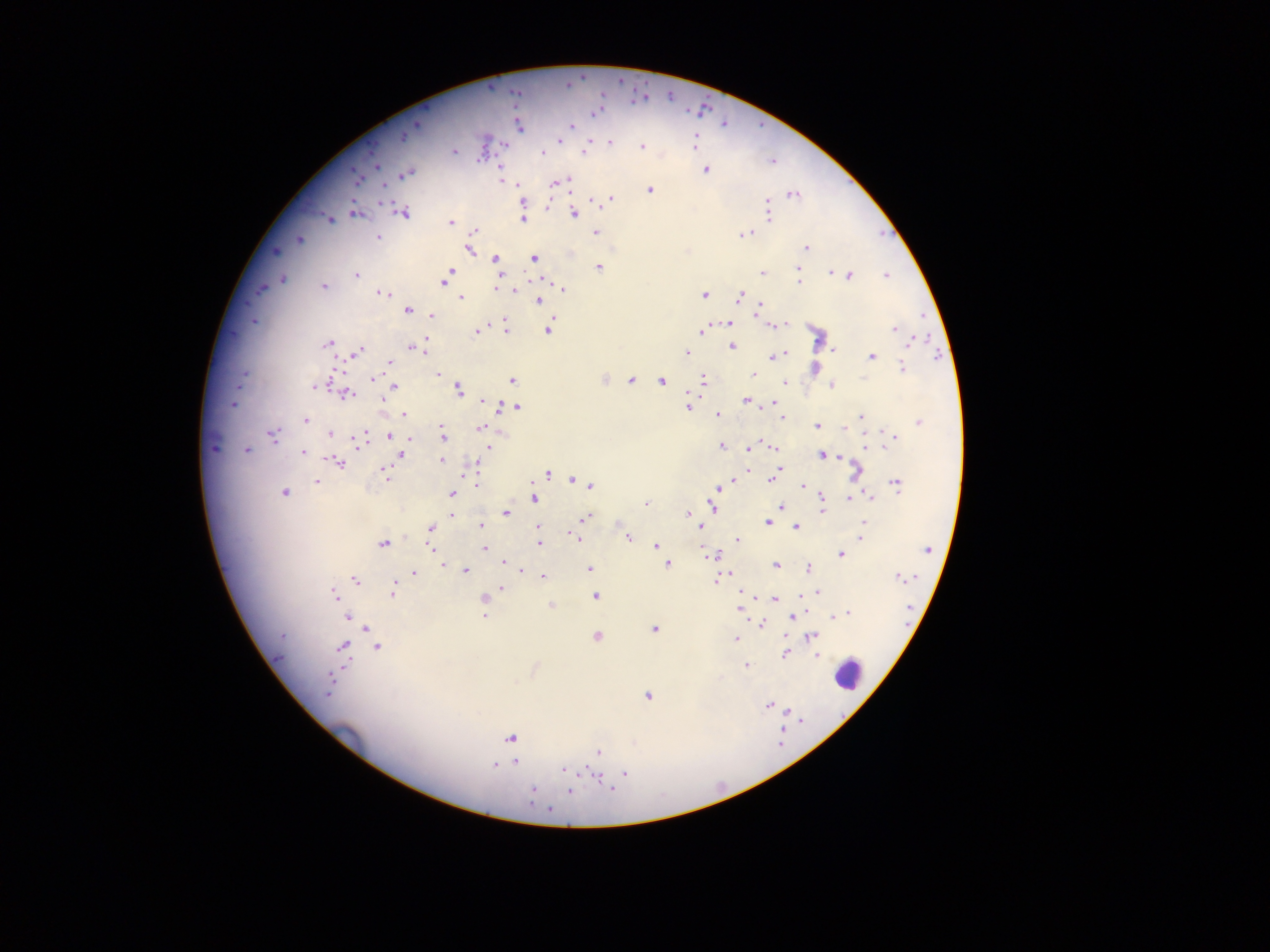
leukocyte locations = approximate centers as [x, y] in pixels: [848, 674]
country = Ghana
capture = mobile-phone photograph through a microscope
preparation = thick blood smear
image size = 1270×952 pixels
field of view = single
malaria parasite locations = approximate centers as [x, y] in pixels: [568, 84], [597, 110], [415, 124], [518, 125], [571, 125], [404, 135], [559, 138], [609, 142], [694, 143], [503, 145], [641, 146], [454, 153], [584, 153], [542, 154], [772, 161], [376, 165], [704, 169], [405, 173], [356, 178], [501, 179], [566, 181], [505, 182], [555, 182], [518, 184], [649, 189], [792, 194], [609, 198], [596, 201], [766, 202], [547, 207], [767, 209], [354, 212], [404, 212], [574, 213], [767, 217], [328, 219], [522, 219], [451, 222], [474, 230], [595, 232], [744, 233], [378, 237], [299, 239], [468, 248], [806, 248], [274, 250], [534, 258], [494, 259], [598, 267], [797, 267], [763, 272], [828, 272], [449, 274], [356, 275], [885, 275], [849, 276], [445, 278], [282, 279], [547, 280], [798, 281], [323, 286], [261, 287], [515, 289], [563, 289], [496, 291], [380, 292], [704, 295], [737, 296], [460, 298], [537, 301], [759, 308], [408, 310], [431, 314], [252, 321], [728, 323], [505, 326], [773, 326], [547, 329], [893, 329], [477, 330], [703, 331], [912, 341], [424, 342], [327, 343], [732, 345], [411, 347], [833, 349], [424, 350], [356, 351], [685, 353], [786, 354], [773, 356], [871, 357], [390, 363], [902, 366], [814, 367], [438, 374], [752, 374], [373, 378], [511, 379], [604, 379], [631, 380], [661, 381], [702, 381], [784, 383], [831, 384], [315, 385], [393, 386], [458, 390], [346, 394], [383, 399], [482, 400], [745, 400], [234, 403], [773, 403], [501, 407], [516, 407], [686, 407], [403, 414], [717, 415], [860, 416], [782, 417], [305, 420], [918, 422], [817, 426], [481, 427], [329, 432], [883, 432], [393, 433], [272, 434], [443, 435], [388, 436], [892, 437], [408, 438], [359, 440], [887, 444], [721, 446], [487, 447], [773, 447], [865, 447], [213, 448], [750, 448], [246, 450], [303, 452], [821, 454], [400, 455], [441, 460], [337, 462], [475, 466], [749, 470], [779, 471], [855, 472], [547, 474], [386, 475], [773, 477], [574, 479], [733, 480], [316, 481], [895, 482], [475, 484], [729, 484], [591, 486], [802, 486], [717, 487], [284, 493], [852, 493], [452, 494], [870, 496], [533, 497], [849, 498], [822, 499], [645, 503], [712, 506], [781, 506], [821, 511], [505, 513], [451, 514], [688, 514], [584, 518], [863, 521], [767, 522], [480, 525], [796, 527], [431, 528], [539, 528], [701, 528], [577, 537], [627, 537], [861, 537], [737, 540], [538, 543], [382, 544], [655, 546], [430, 549], [485, 549], [927, 549], [716, 554], [841, 554], [711, 555], [504, 562], [667, 563], [442, 565], [775, 565], [806, 568], [521, 569], [589, 569], [465, 570], [414, 573], [543, 577], [899, 577], [718, 578], [356, 579], [502, 589], [393, 591], [818, 592], [333, 595], [799, 595], [595, 596], [774, 598], [484, 599], [551, 606], [740, 609], [847, 613], [485, 615], [837, 615], [348, 616], [791, 616], [831, 617], [761, 624], [366, 628], [653, 628], [282, 636], [596, 636], [809, 636], [735, 640], [377, 647], [342, 648], [786, 653], [817, 655], [745, 665], [329, 681], [646, 695], [769, 704], [510, 738], [599, 751], [516, 761], [495, 766], [563, 769], [623, 774], [532, 790], [570, 790]